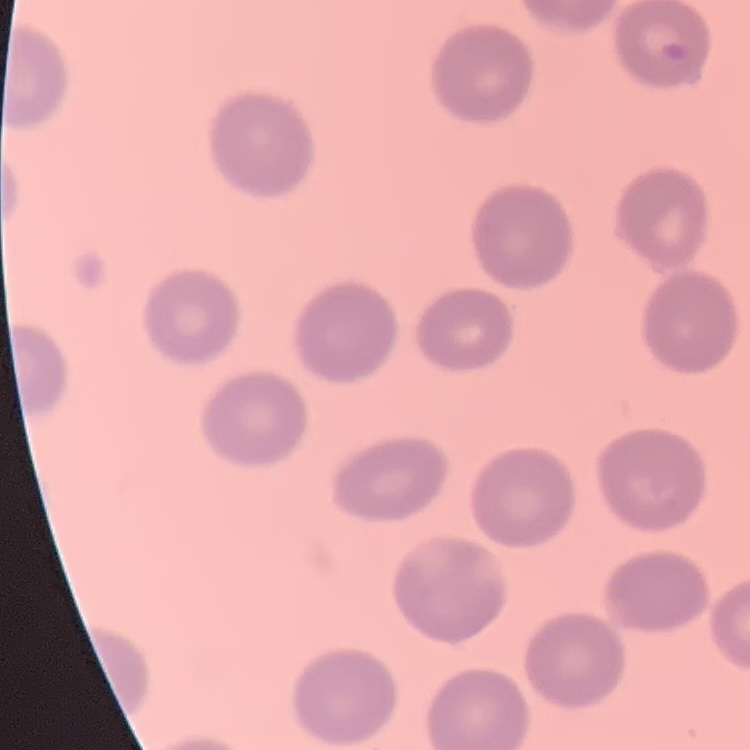
erythrocyte morphology = no rouleaux formation
image type = one tile cut from a larger photomicrograph
preparation = thin peripheral smear
stain = Field's or Giemsa